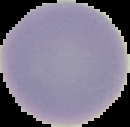

image size = 130×127 pixels
result = negative for Plasmodium parasites
image type = segmented cell region on a black background
preparation = thin blood smear